Locate and identify every blood parasite.
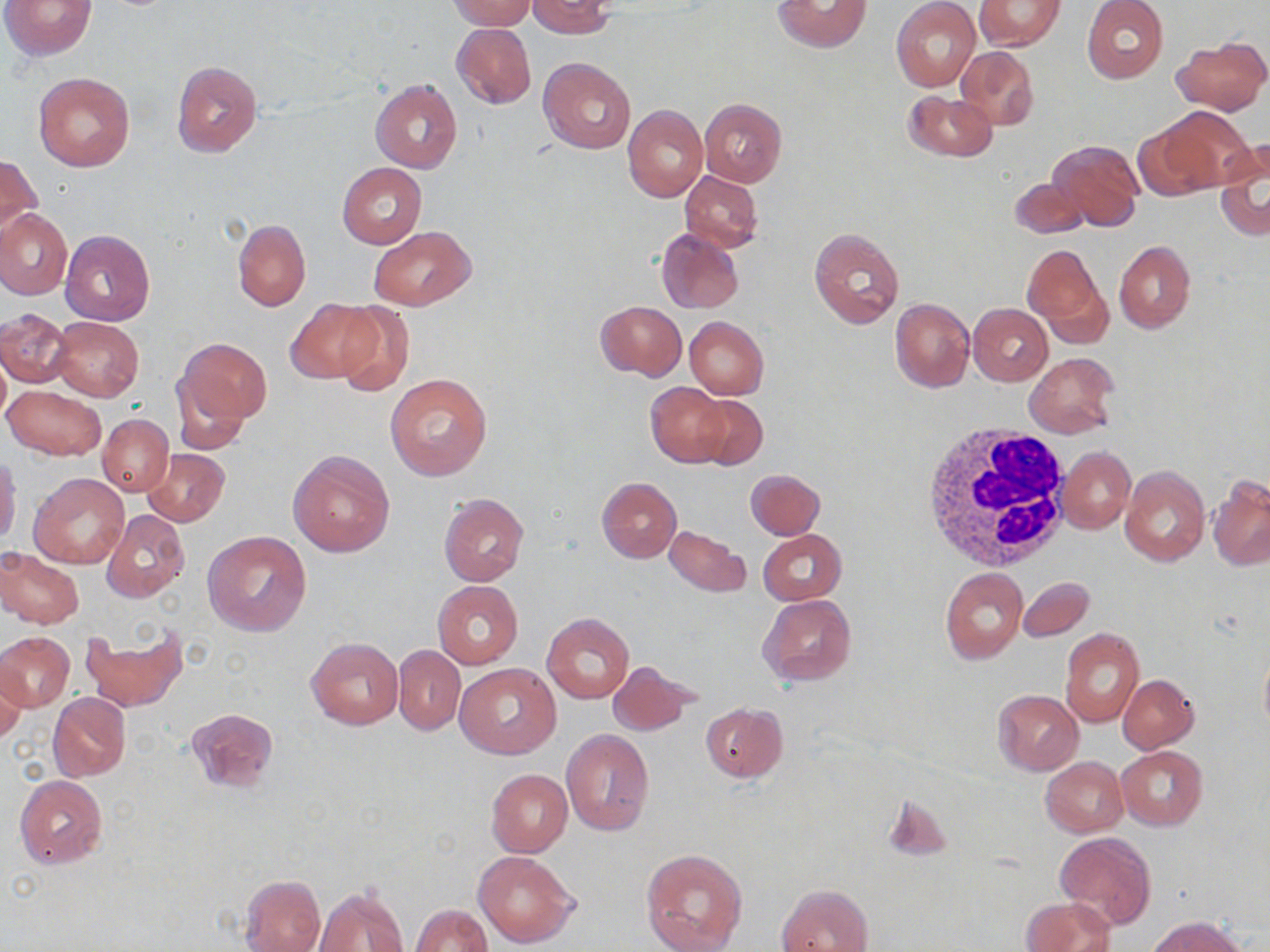
No blood parasites observed.

Approximate bounding boxes as named x1/y1/x2/y2 corners in pixels. White blood cell locations: (x1=915, y1=422, x2=1071, y2=572). Uninfected red blood cell locations: (x1=2, y1=0, x2=97, y2=60), (x1=447, y1=0, x2=536, y2=31), (x1=527, y1=0, x2=615, y2=38), (x1=772, y1=0, x2=871, y2=52), (x1=975, y1=0, x2=1066, y2=51), (x1=1081, y1=0, x2=1168, y2=83), (x1=891, y1=1, x2=981, y2=91), (x1=452, y1=23, x2=536, y2=108), (x1=1175, y1=38, x2=1268, y2=114), (x1=954, y1=44, x2=1038, y2=133), (x1=538, y1=56, x2=636, y2=154), (x1=172, y1=61, x2=261, y2=156), (x1=34, y1=73, x2=134, y2=171), (x1=370, y1=78, x2=462, y2=173), (x1=903, y1=92, x2=997, y2=161), (x1=699, y1=98, x2=787, y2=185), (x1=623, y1=105, x2=708, y2=203), (x1=1149, y1=108, x2=1251, y2=193), (x1=1132, y1=125, x2=1213, y2=201), (x1=1049, y1=140, x2=1144, y2=232), (x1=1216, y1=141, x2=1269, y2=241), (x1=1, y1=154, x2=40, y2=240), (x1=338, y1=163, x2=426, y2=247), (x1=680, y1=172, x2=763, y2=252), (x1=1009, y1=176, x2=1088, y2=240), (x1=0, y1=209, x2=72, y2=299), (x1=232, y1=219, x2=311, y2=311), (x1=368, y1=227, x2=476, y2=309), (x1=656, y1=227, x2=744, y2=314), (x1=809, y1=228, x2=905, y2=330), (x1=60, y1=230, x2=155, y2=326), (x1=1114, y1=240, x2=1195, y2=332), (x1=1023, y1=244, x2=1102, y2=331), (x1=284, y1=297, x2=386, y2=385), (x1=890, y1=297, x2=974, y2=391), (x1=331, y1=301, x2=415, y2=394), (x1=596, y1=301, x2=686, y2=380), (x1=968, y1=303, x2=1052, y2=385), (x1=0, y1=308, x2=74, y2=388), (x1=51, y1=317, x2=144, y2=402), (x1=684, y1=317, x2=769, y2=400), (x1=174, y1=337, x2=271, y2=434), (x1=1025, y1=352, x2=1118, y2=438), (x1=385, y1=373, x2=492, y2=479), (x1=646, y1=382, x2=729, y2=467), (x1=3, y1=384, x2=105, y2=461), (x1=692, y1=394, x2=767, y2=471), (x1=98, y1=414, x2=173, y2=497), (x1=1058, y1=447, x2=1135, y2=533), (x1=144, y1=448, x2=230, y2=527), (x1=288, y1=450, x2=395, y2=556), (x1=0, y1=456, x2=21, y2=547), (x1=1119, y1=464, x2=1210, y2=567), (x1=745, y1=468, x2=825, y2=539), (x1=30, y1=473, x2=129, y2=568), (x1=1208, y1=475, x2=1270, y2=571), (x1=597, y1=477, x2=681, y2=562), (x1=438, y1=494, x2=529, y2=587), (x1=102, y1=510, x2=190, y2=602), (x1=665, y1=525, x2=748, y2=596), (x1=758, y1=529, x2=846, y2=605), (x1=203, y1=531, x2=312, y2=637), (x1=0, y1=547, x2=83, y2=629), (x1=940, y1=567, x2=1028, y2=663), (x1=1018, y1=576, x2=1094, y2=642), (x1=433, y1=580, x2=523, y2=668), (x1=757, y1=594, x2=856, y2=686), (x1=542, y1=613, x2=635, y2=703), (x1=81, y1=627, x2=188, y2=713), (x1=1060, y1=627, x2=1145, y2=728), (x1=0, y1=631, x2=74, y2=711), (x1=306, y1=637, x2=403, y2=730), (x1=393, y1=645, x2=465, y2=735), (x1=1258, y1=647, x2=1270, y2=740), (x1=0, y1=658, x2=26, y2=742), (x1=607, y1=660, x2=696, y2=737), (x1=454, y1=663, x2=560, y2=759), (x1=1118, y1=675, x2=1198, y2=752), (x1=993, y1=690, x2=1083, y2=776), (x1=49, y1=692, x2=131, y2=780), (x1=700, y1=703, x2=787, y2=782), (x1=187, y1=707, x2=278, y2=792), (x1=562, y1=729, x2=654, y2=835), (x1=1117, y1=746, x2=1207, y2=830), (x1=1040, y1=757, x2=1128, y2=837), (x1=485, y1=768, x2=571, y2=857), (x1=14, y1=775, x2=108, y2=868), (x1=1055, y1=831, x2=1157, y2=929), (x1=640, y1=848, x2=748, y2=952), (x1=474, y1=851, x2=578, y2=948), (x1=238, y1=874, x2=326, y2=952), (x1=776, y1=883, x2=874, y2=952), (x1=314, y1=887, x2=408, y2=952), (x1=1022, y1=897, x2=1117, y2=952), (x1=410, y1=904, x2=493, y2=951), (x1=1150, y1=916, x2=1248, y2=952). Slide-level diagnosis: negative for blood parasites. May-Grünwald-Giemsa stain. Captured at 1000x magnification. Image is 1270×952 pixels. Light microscopy. One field of a larger specimen. Thin blood smear.